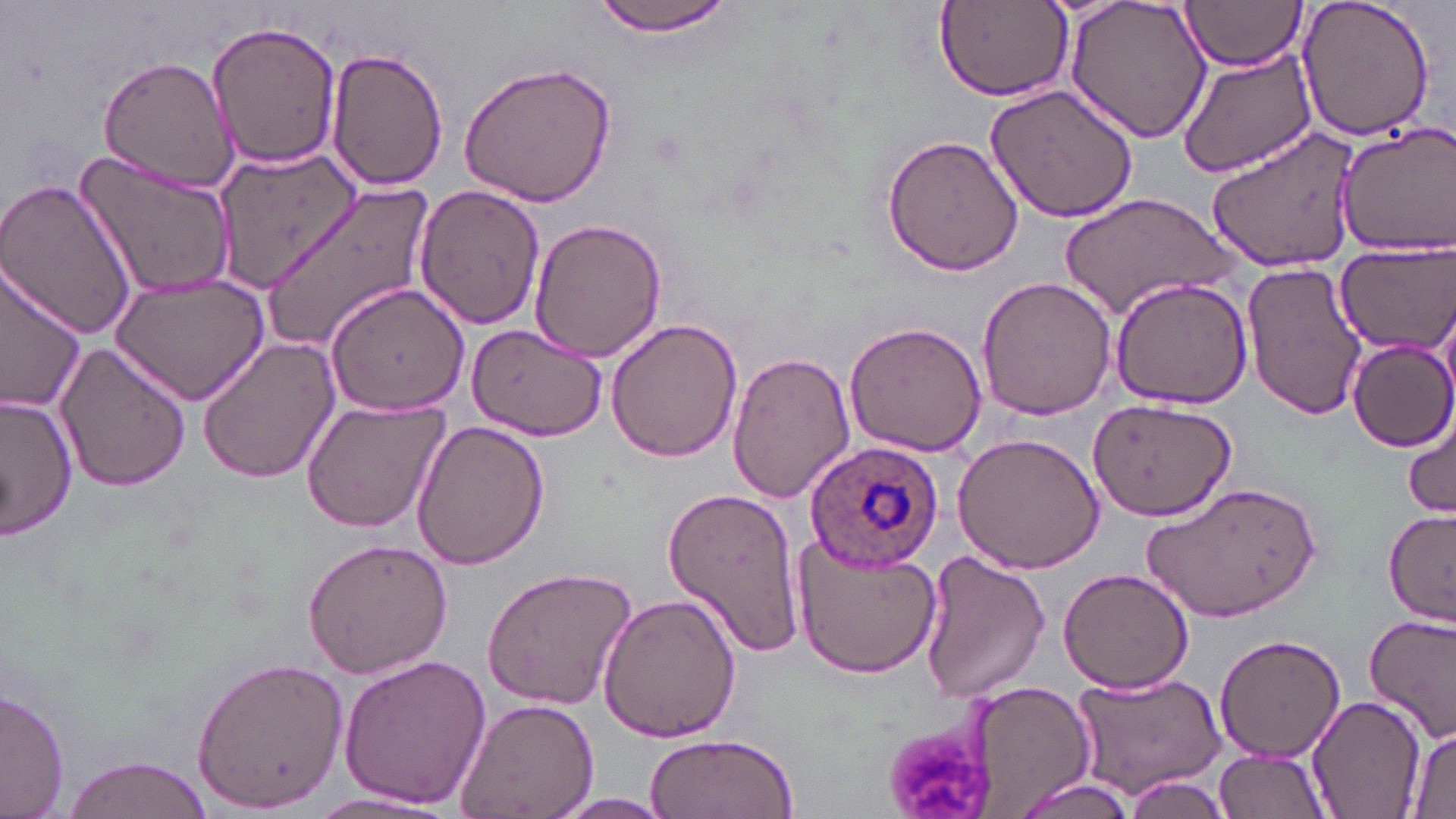

slide-level diagnosis = Plasmodium ovale
stain = May-Grünwald-Giemsa
magnification = 1000x
modality = optical microscopy
field of view = one of a larger specimen
Plasmodium ovale-infected red blood cell locations = approximate bounding boxes as (x1, y1, x2, y2) in pixels: (803, 440, 943, 576)
platelet locations = approximate bounding boxes as (x1, y1, x2, y2) in pixels: (883, 723, 990, 814)
uninfected red blood cell locations = approximate bounding boxes as (x1, y1, x2, y2) in pixels: (591, 0, 739, 40), (1062, 0, 1215, 144), (1180, 0, 1308, 72), (1294, 0, 1439, 143), (934, 1, 1074, 101), (206, 19, 342, 171), (1175, 41, 1318, 179), (326, 48, 448, 192), (97, 55, 241, 194), (457, 60, 619, 209), (985, 80, 1142, 224), (1333, 123, 1456, 256), (1204, 125, 1365, 272), (883, 132, 1024, 275), (74, 143, 242, 302), (0, 175, 138, 339), (260, 181, 436, 349), (414, 183, 546, 331), (1061, 193, 1236, 319), (527, 217, 666, 364), (1334, 239, 1453, 352), (1243, 259, 1367, 421), (0, 261, 88, 414), (110, 272, 270, 405), (978, 274, 1118, 420), (1112, 277, 1252, 409), (324, 282, 471, 417), (606, 318, 742, 464), (464, 320, 609, 441), (844, 320, 988, 457), (196, 336, 342, 485), (52, 338, 190, 493), (1346, 338, 1456, 452), (728, 350, 854, 502), (0, 395, 78, 542), (1083, 396, 1240, 522), (299, 399, 449, 535), (1403, 406, 1455, 519), (412, 421, 550, 569), (951, 434, 1103, 575), (1143, 482, 1322, 621), (661, 485, 807, 661), (1382, 507, 1456, 625), (302, 537, 454, 678), (792, 537, 940, 680), (920, 551, 1049, 701), (481, 566, 638, 709), (1056, 566, 1197, 694), (595, 592, 743, 745), (1364, 612, 1456, 742), (1213, 634, 1347, 764), (335, 653, 491, 811), (191, 655, 349, 811), (1068, 670, 1227, 797), (962, 681, 1096, 819), (0, 686, 70, 818), (1309, 696, 1425, 817), (452, 697, 599, 819), (1404, 727, 1456, 816), (646, 731, 801, 819), (1213, 749, 1334, 819), (57, 754, 217, 819), (1122, 776, 1233, 818), (301, 790, 456, 816), (551, 792, 681, 817)
preparation = thin blood film
image size = 1456×819 pixels